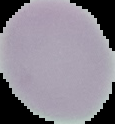

preparation = thin blood smear
malaria status = uninfected
image size = 115×124 pixels
image type = segmented cell region on a black background